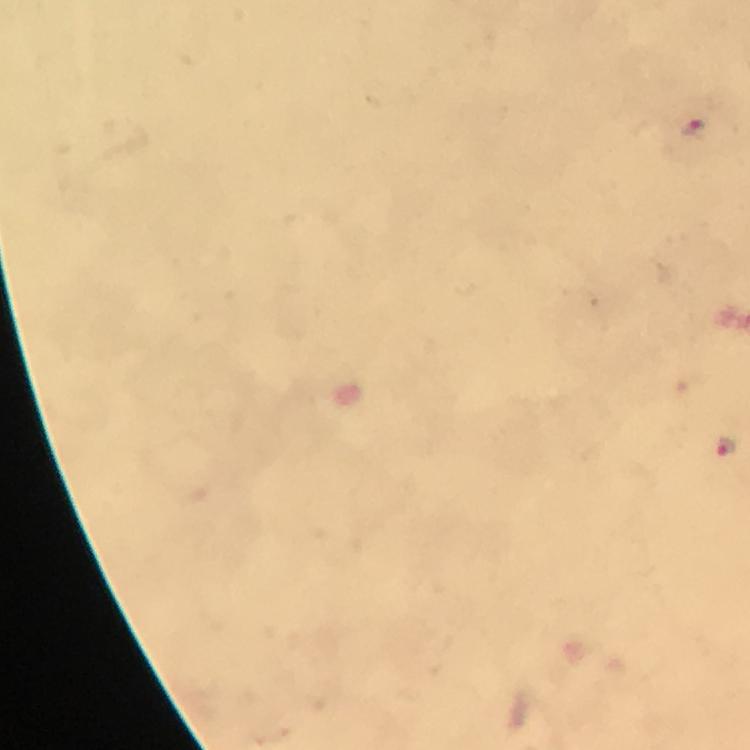
immersion_oil: used
cropped_from: one field of view
capture: smartphone mounted on the microscope
stain: Giemsa
magnification: 100x
malaria_parasite_locations: 'approximate centers as (x, y) in pixels: (694, 128), (727, 446)'
context: from a diagnostic examination for malaria
preparation: thick blood film
image_size: 750×750 pixels